Outline each blood parasite and name the species.
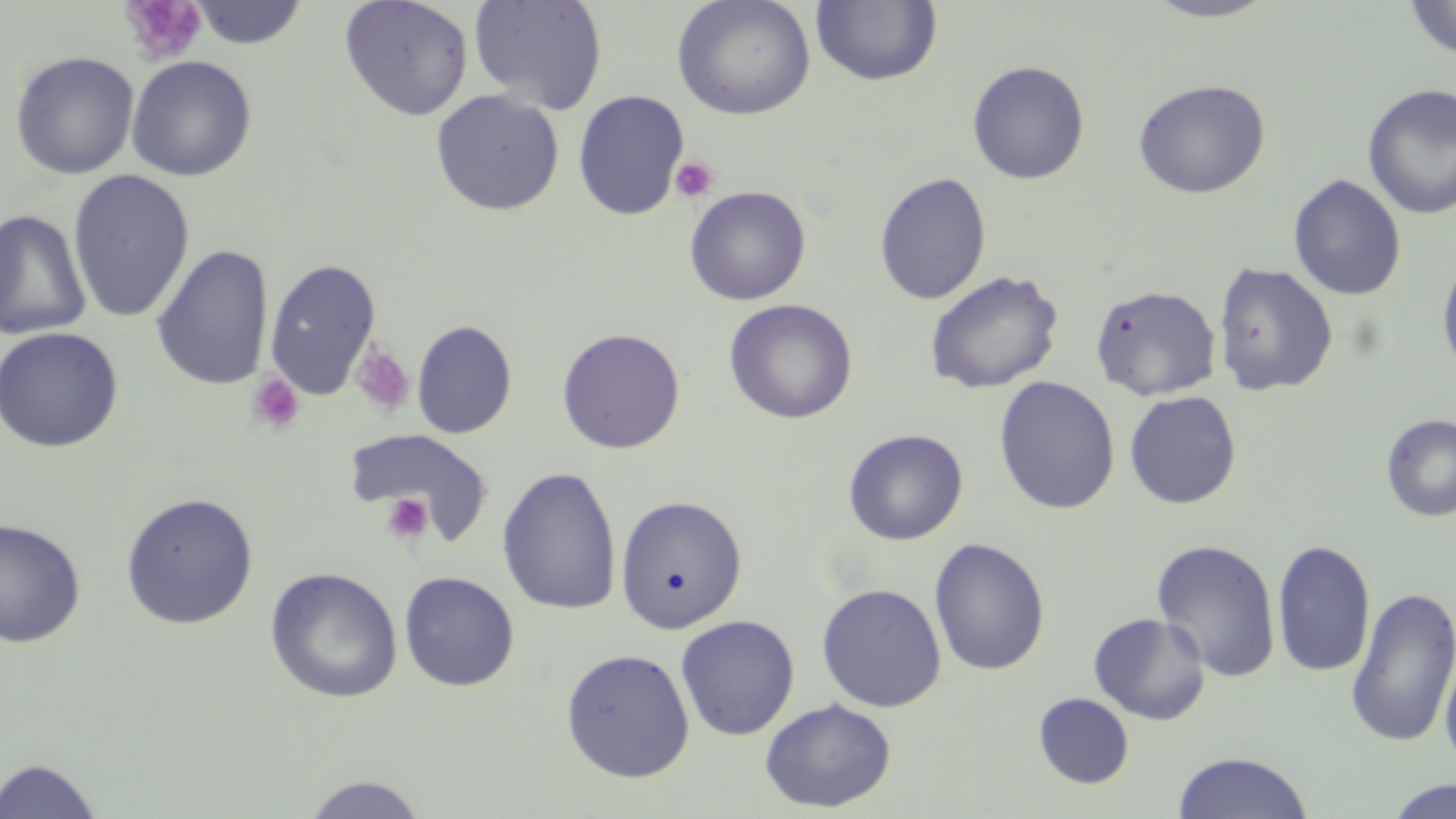

No blood parasites observed.

slide-level diagnosis = negative for blood parasites
preparation = thin blood smear
uninfected red blood cell locations = approximate bounding boxes as (x1,y1)-(x2,y2) corner pairs in pixels: (339,0)-(474,121), (469,0)-(609,114), (672,0)-(815,120), (1142,0)-(1278,22), (1403,0)-(1456,61), (187,1)-(309,49), (811,1)-(942,87), (10,51)-(139,180), (126,55)-(257,182), (966,60)-(1090,184), (1133,79)-(1270,198), (1362,83)-(1456,220), (429,89)-(564,215), (572,89)-(690,220), (67,169)-(195,323), (874,172)-(992,306), (1288,174)-(1407,301), (684,186)-(811,305), (0,209)-(92,341), (151,243)-(274,391), (1437,255)-(1456,379), (263,257)-(382,400), (1213,262)-(1338,397), (925,270)-(1063,394), (1090,283)-(1222,401), (723,299)-(858,424), (411,319)-(517,439), (0,326)-(124,453), (556,327)-(685,454), (993,376)-(1120,514), (1123,390)-(1242,509), (1380,414)-(1456,522), (344,428)-(493,543), (843,428)-(968,545), (497,466)-(622,615), (120,491)-(258,629), (615,495)-(748,633), (0,517)-(86,649), (928,537)-(1050,676), (1271,538)-(1376,678), (1150,539)-(1281,682), (264,566)-(403,703), (398,571)-(520,692), (816,582)-(947,712), (1345,586)-(1456,749), (1088,612)-(1211,725), (674,614)-(800,740), (560,647)-(695,783), (1439,649)-(1456,775), (1033,693)-(1134,789), (760,697)-(896,812), (1172,751)-(1314,818), (0,757)-(104,818), (299,774)-(430,818), (1383,779)-(1456,819)
stain = May-Grünwald-Giemsa
platelet locations = approximate bounding boxes as (x1,y1)-(x2,y2) corner pairs in pixels: (119,0)-(208,67), (670,156)-(719,203), (350,341)-(416,418), (245,372)-(305,437), (360,450)-(472,546), (381,492)-(434,544)
image size = 1456×819 pixels
magnification = 1000x
field of view = single
modality = optical microscopy